Comment on the morphology of the red blood cells.
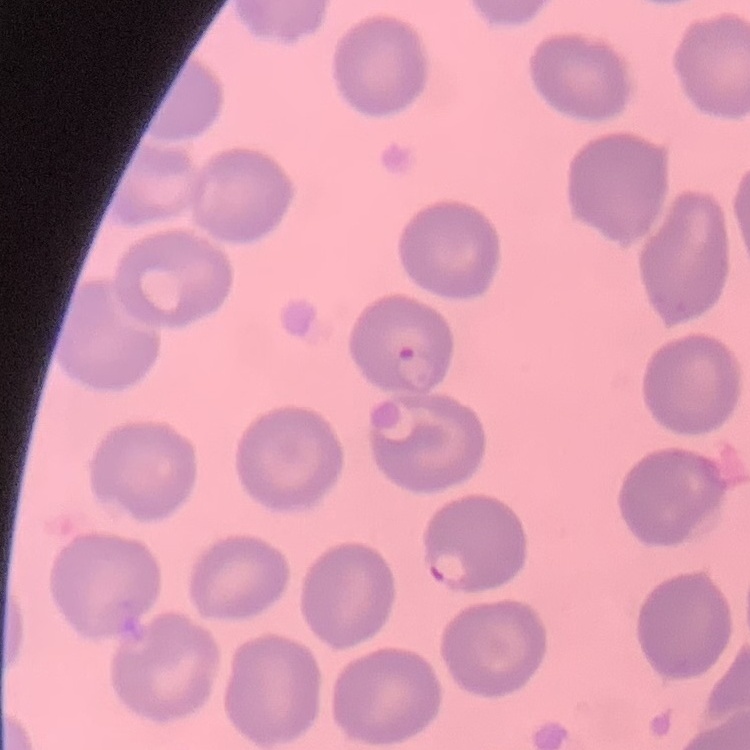
They show no rouleaux formation.

Square crop of a larger photomicrograph. Thin blood film. Field's or Giemsa stain.